Report the malaria status.
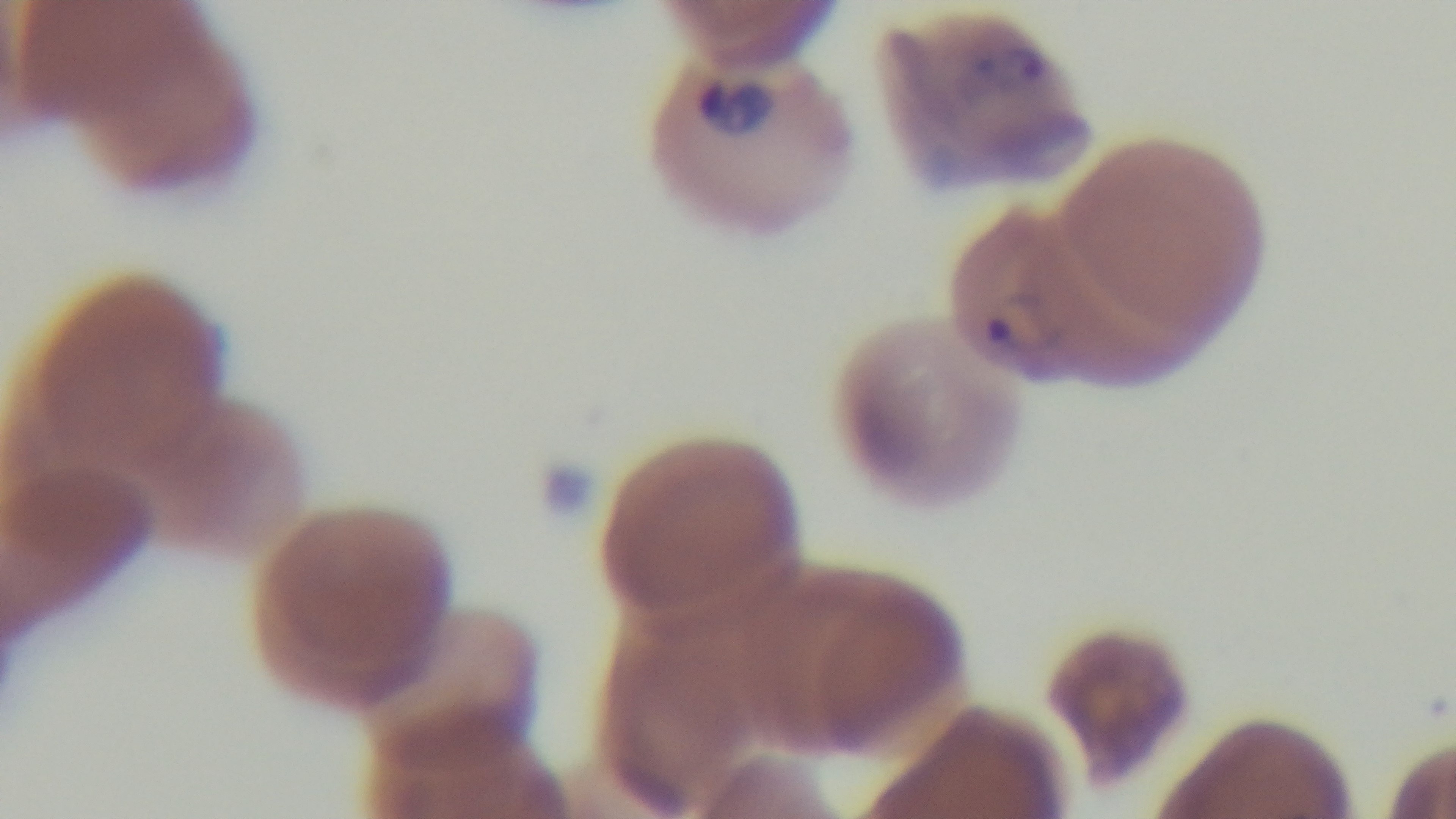
It is infected.

Summary:
  - Field of view: one from the slide
  - Objective: 100x oil immersion
  - Modality: light microscopy
  - Stain: Giemsa
  - Preparation: thin smear
  - Capture: mounted 4K digital camera